Give the preparation type.
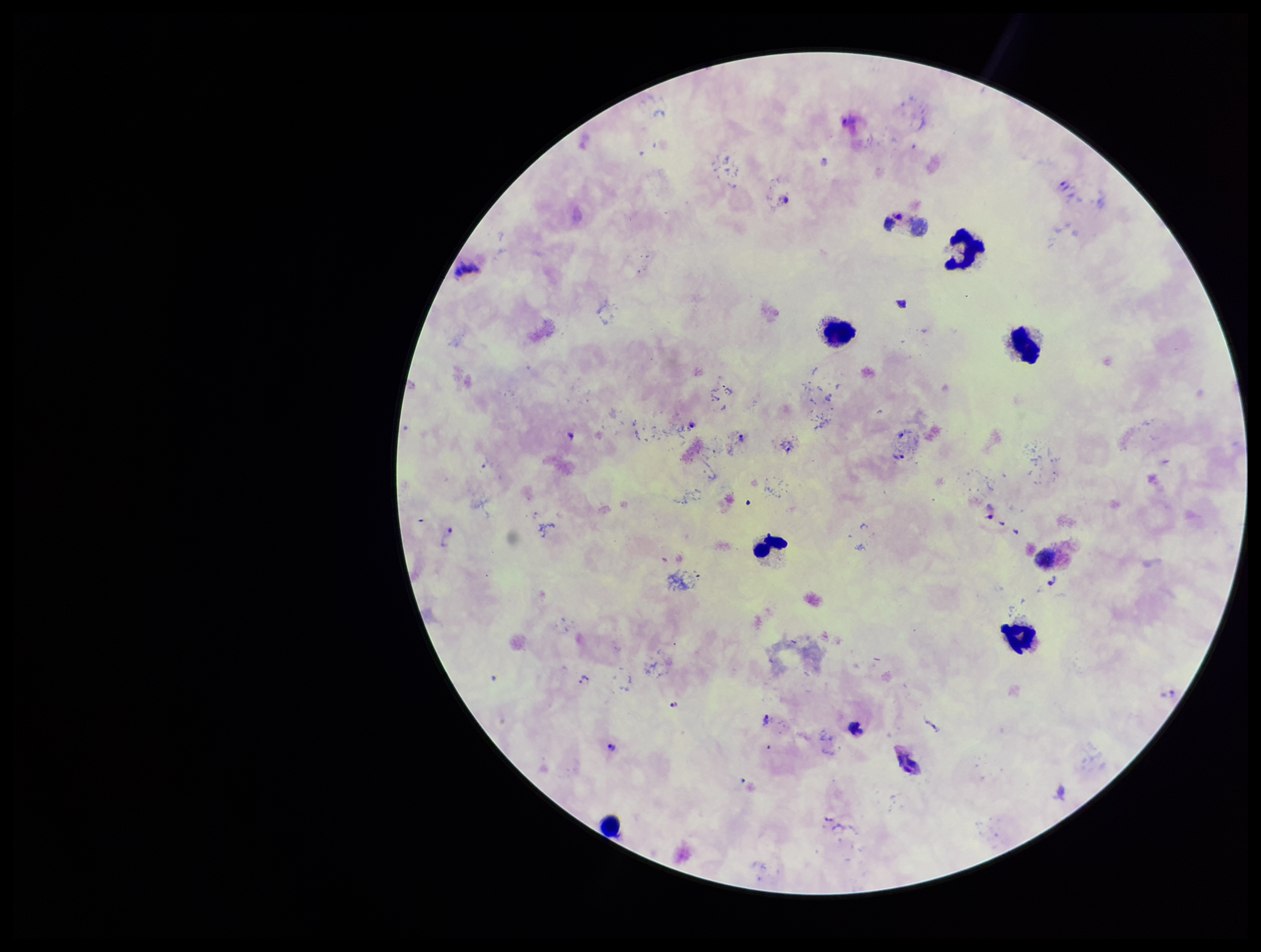

A thick smear.

Stained with Giemsa. Patient malaria status: positive. Parasite count: 15. One field from this slide. Photographed through the microscope eyepiece with a smartphone camera. Species reported for this patient: Plasmodium vivax. Plasmodium parasites: seen. Leukocyte count: 7. Image is 1261×952 pixels.